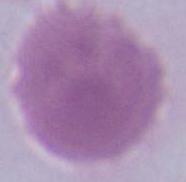

Summary:
  - Modality: micrograph
  - Identification: red blood cell
  - Magnification: 1000x